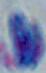
{
  "modality": "photomicrograph",
  "identification": "Toxoplasma gondii",
  "magnification": "1000x"
}